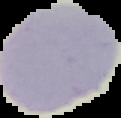
image_type: cell region segmented out of the field of view; surrounding area masked to black
image_size: 121×118 pixels
preparation: thin blood smear
result: negative for malaria parasites